Give the position of every leukocyte.
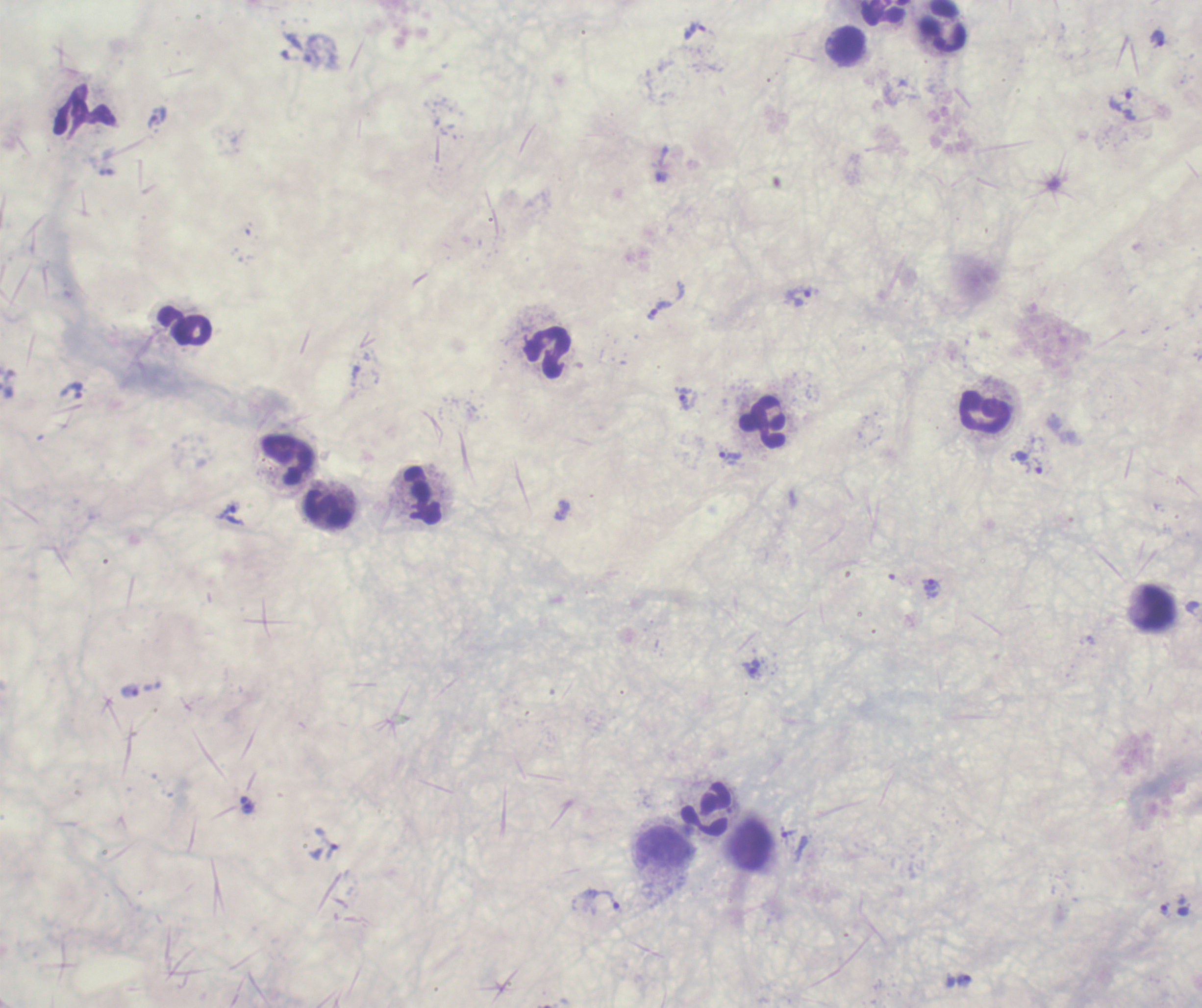

Approximate centers as (x, y) in pixels.
Leukocytes: (886, 13), (943, 25), (845, 44), (186, 326), (549, 352), (986, 411), (763, 422), (288, 460), (422, 496), (327, 508), (1154, 607), (705, 808), (663, 846).

Approximate centers as (x, y) in pixels.
Summary:
  - Trophozoite locations: (694, 31), (1158, 38), (311, 56), (1120, 100), (158, 117), (798, 296), (659, 311), (73, 391), (688, 399), (730, 456), (1038, 466), (562, 511), (230, 515), (931, 585), (752, 669), (131, 691), (248, 808), (788, 832), (332, 852), (602, 900), (1165, 909), (964, 980)
  - Field of view: one from this slide
  - Image size: 1202×1008 pixels
  - Magnification: 100x
  - Result: malaria parasites identified
  - Preparation: thick blood smear
  - Context: previously used in a real diagnosis
  - Stain: Romanowsky
  - Background quality: unsatisfactory
  - Coloration quality: bad